Locate every blood parasite and identify its species.
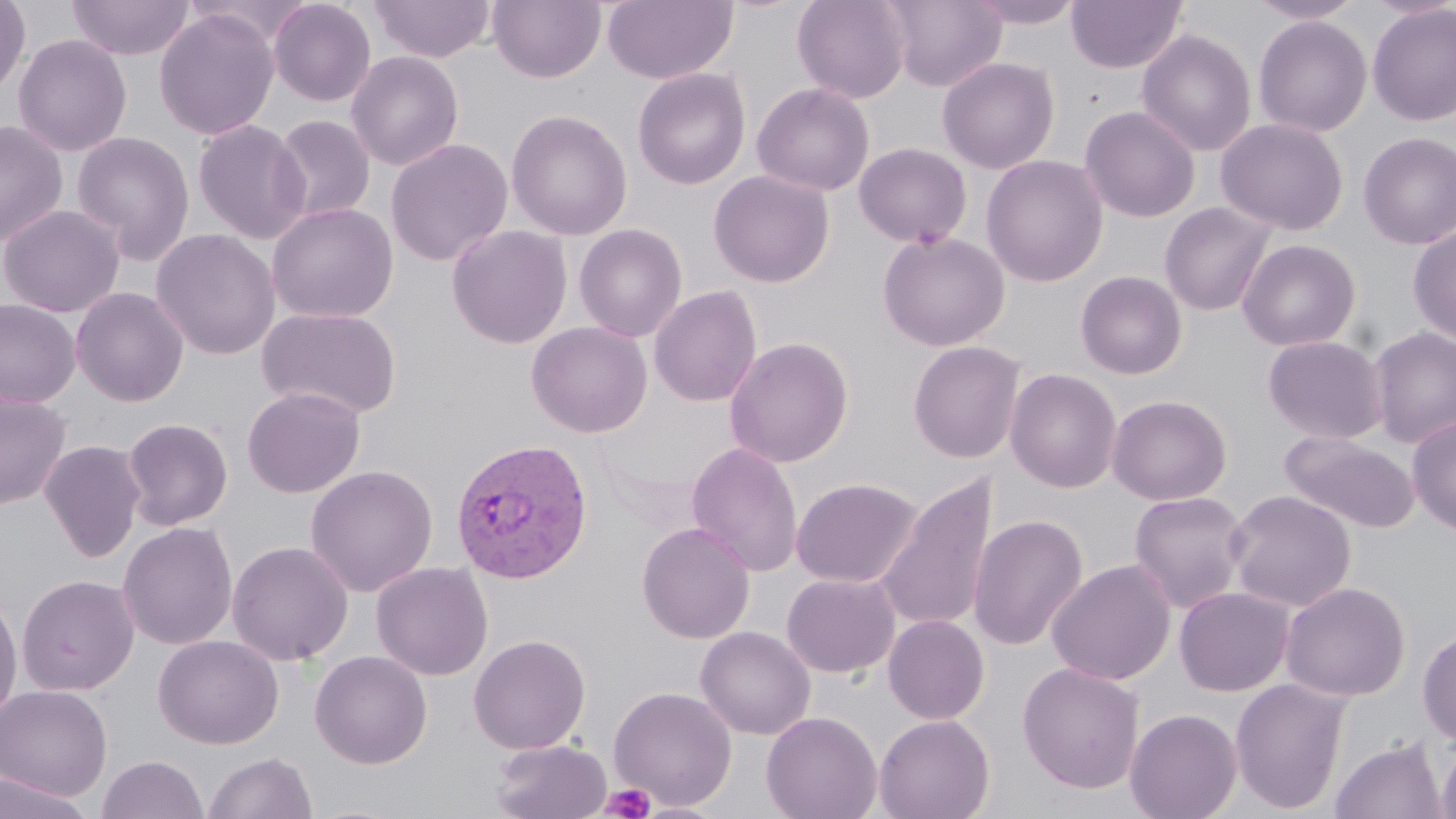

Approximate bounding boxes as named x1/y1/x2/y2 corners in pixels.
Plasmodium vivax-infected red blood cells: (x1=449, y1=438, x2=594, y2=585).
No Plasmodium falciparum, Plasmodium ovale, Plasmodium malariae, Babesia divergens, or Trypanosoma brucei observed.

Uninfected red blood cell locations: (x1=0, y1=0, x2=31, y2=99), (x1=67, y1=0, x2=195, y2=61), (x1=268, y1=0, x2=376, y2=107), (x1=368, y1=0, x2=496, y2=63), (x1=488, y1=0, x2=606, y2=84), (x1=602, y1=0, x2=738, y2=85), (x1=792, y1=0, x2=911, y2=103), (x1=881, y1=0, x2=1006, y2=91), (x1=966, y1=0, x2=1087, y2=29), (x1=1066, y1=0, x2=1188, y2=73), (x1=1247, y1=0, x2=1365, y2=24), (x1=1367, y1=4, x2=1456, y2=126), (x1=154, y1=8, x2=280, y2=141), (x1=1253, y1=15, x2=1372, y2=137), (x1=1136, y1=29, x2=1257, y2=157), (x1=13, y1=34, x2=132, y2=156), (x1=346, y1=51, x2=465, y2=171), (x1=937, y1=56, x2=1059, y2=174), (x1=632, y1=67, x2=751, y2=190), (x1=752, y1=82, x2=875, y2=197), (x1=1080, y1=106, x2=1200, y2=222), (x1=505, y1=108, x2=633, y2=241), (x1=271, y1=114, x2=375, y2=223), (x1=1215, y1=117, x2=1349, y2=235), (x1=0, y1=119, x2=69, y2=248), (x1=192, y1=119, x2=312, y2=244), (x1=71, y1=131, x2=195, y2=264), (x1=1358, y1=132, x2=1456, y2=250), (x1=385, y1=138, x2=514, y2=266), (x1=854, y1=142, x2=972, y2=248), (x1=981, y1=155, x2=1108, y2=288), (x1=708, y1=170, x2=834, y2=288), (x1=1159, y1=201, x2=1277, y2=317), (x1=266, y1=202, x2=399, y2=323), (x1=0, y1=204, x2=124, y2=318), (x1=573, y1=223, x2=688, y2=342), (x1=446, y1=224, x2=573, y2=349), (x1=1407, y1=226, x2=1456, y2=344), (x1=151, y1=228, x2=281, y2=360), (x1=877, y1=231, x2=1010, y2=351), (x1=1236, y1=238, x2=1361, y2=352), (x1=1075, y1=270, x2=1188, y2=379), (x1=649, y1=285, x2=762, y2=406), (x1=70, y1=287, x2=189, y2=407), (x1=0, y1=297, x2=81, y2=408), (x1=255, y1=306, x2=404, y2=420), (x1=526, y1=321, x2=653, y2=438), (x1=1368, y1=326, x2=1456, y2=448), (x1=1262, y1=335, x2=1388, y2=443), (x1=724, y1=336, x2=854, y2=468), (x1=908, y1=341, x2=1026, y2=463), (x1=1005, y1=368, x2=1122, y2=493), (x1=242, y1=386, x2=366, y2=498), (x1=0, y1=391, x2=72, y2=510), (x1=1106, y1=394, x2=1232, y2=505), (x1=1406, y1=416, x2=1456, y2=536), (x1=121, y1=417, x2=233, y2=531), (x1=1278, y1=431, x2=1419, y2=533), (x1=40, y1=440, x2=147, y2=563), (x1=686, y1=441, x2=804, y2=577), (x1=305, y1=464, x2=438, y2=597), (x1=876, y1=473, x2=998, y2=634), (x1=790, y1=477, x2=922, y2=588), (x1=1225, y1=489, x2=1357, y2=612), (x1=1128, y1=491, x2=1251, y2=613), (x1=968, y1=515, x2=1088, y2=651), (x1=636, y1=521, x2=756, y2=644), (x1=117, y1=522, x2=238, y2=650), (x1=226, y1=540, x2=354, y2=665), (x1=1046, y1=559, x2=1176, y2=686), (x1=371, y1=561, x2=494, y2=680), (x1=781, y1=572, x2=900, y2=678), (x1=16, y1=573, x2=139, y2=697), (x1=1279, y1=581, x2=1411, y2=702), (x1=1174, y1=586, x2=1294, y2=696), (x1=0, y1=589, x2=24, y2=727), (x1=883, y1=614, x2=989, y2=724), (x1=695, y1=626, x2=815, y2=739), (x1=1417, y1=628, x2=1456, y2=745), (x1=468, y1=633, x2=591, y2=755), (x1=153, y1=634, x2=284, y2=749), (x1=310, y1=650, x2=433, y2=769), (x1=1017, y1=662, x2=1145, y2=794), (x1=1229, y1=676, x2=1351, y2=814), (x1=0, y1=684, x2=113, y2=801), (x1=608, y1=686, x2=738, y2=810), (x1=1124, y1=708, x2=1243, y2=819), (x1=761, y1=711, x2=883, y2=819), (x1=873, y1=714, x2=995, y2=819), (x1=1329, y1=737, x2=1447, y2=819), (x1=1436, y1=737, x2=1456, y2=819), (x1=490, y1=738, x2=612, y2=819), (x1=203, y1=751, x2=317, y2=819), (x1=96, y1=754, x2=208, y2=818), (x1=0, y1=771, x2=95, y2=818), (x1=636, y1=803, x2=725, y2=819). Platelet locations: (x1=600, y1=783, x2=655, y2=819). Slide-level diagnosis: Plasmodium vivax. Thin blood smear. May-Grünwald-Giemsa stain. 1000x magnification. Image is 1456×819 pixels. Optical microscopy. One field of a larger specimen.